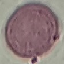 Malaria status: uninfected. Giemsa-stained preparation. Photographed with a smartphone camera at the microscope eyepiece. Thin blood film. Automatically extracted cell patch, resized to 64 × 64 pixels.